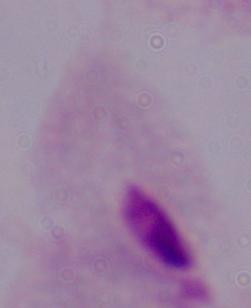 Photomicrograph. A trichomonad is shown. Captured at 1000x magnification.